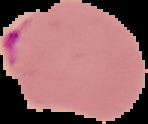

Summary:
  - Preparation: thin blood film
  - Malaria status: parasitized
  - Image size: 148×124 pixels
  - Image type: segmented cell region on a black background